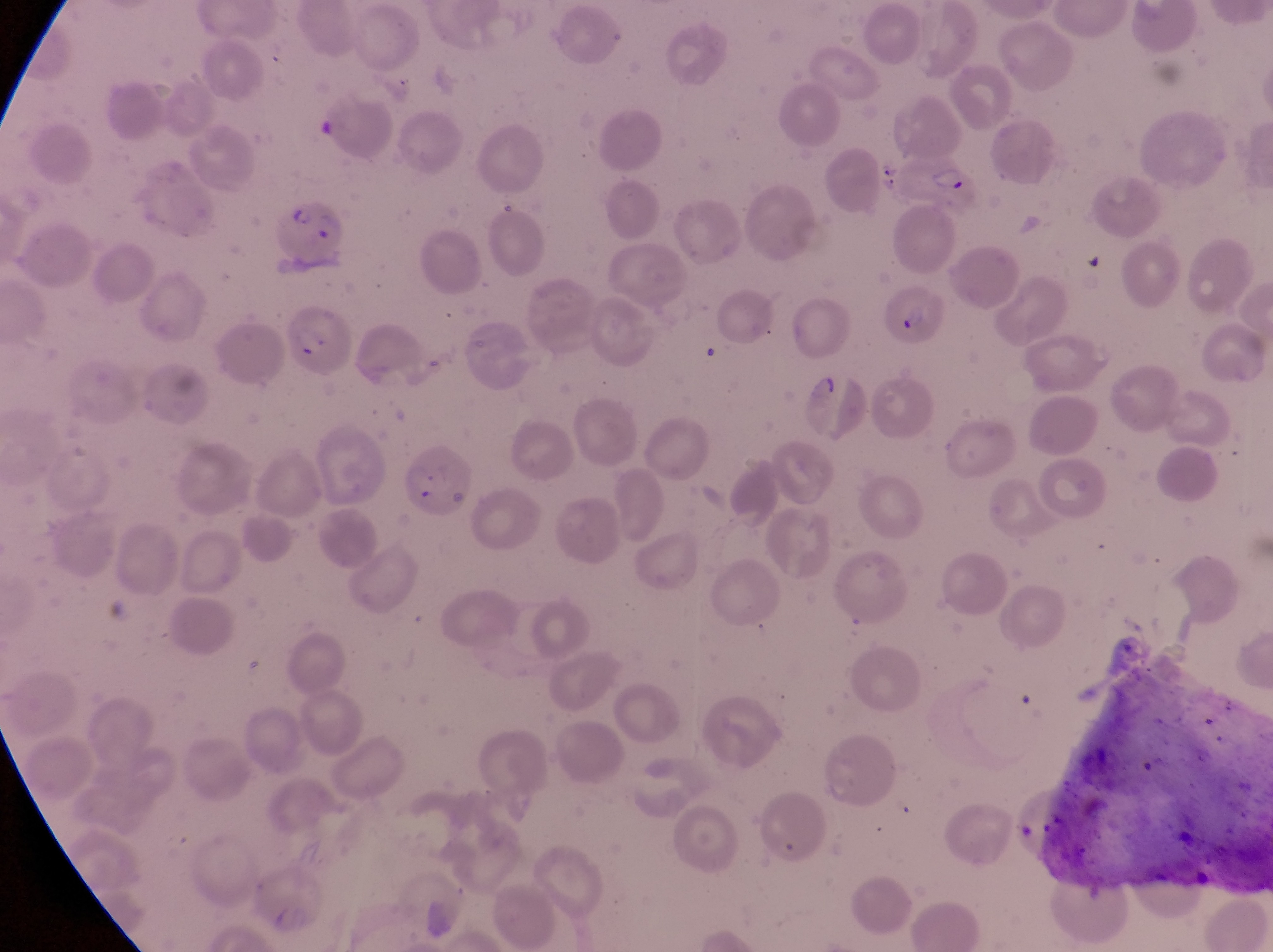

Approximate bounding boxes as left top right bottom in pixels. Parasitised red blood cell locations: 894 150 982 217; 274 199 349 274; 882 285 949 350; 289 312 352 386. Sample from Uganda. Image is 1273×952 pixels. Photographed through the eyepiece of an Olympus CX-23 microscope with a smartphone camera. Single field of view. Magnification of 1000x. Thin blood film.